Name the parasite shown.
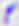
Toxoplasma gondii.

Micrograph. 400x magnification.